State which parasite is depicted.
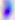

This is Toxoplasma gondii.

Photomicrograph. Captured at 400x magnification.